Report the malaria status of this cell.
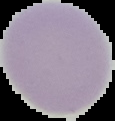
It is uninfected.

Summary:
  - Preparation: thin blood smear
  - Image type: segmented cell region on a black background
  - Image size: 115×121 pixels